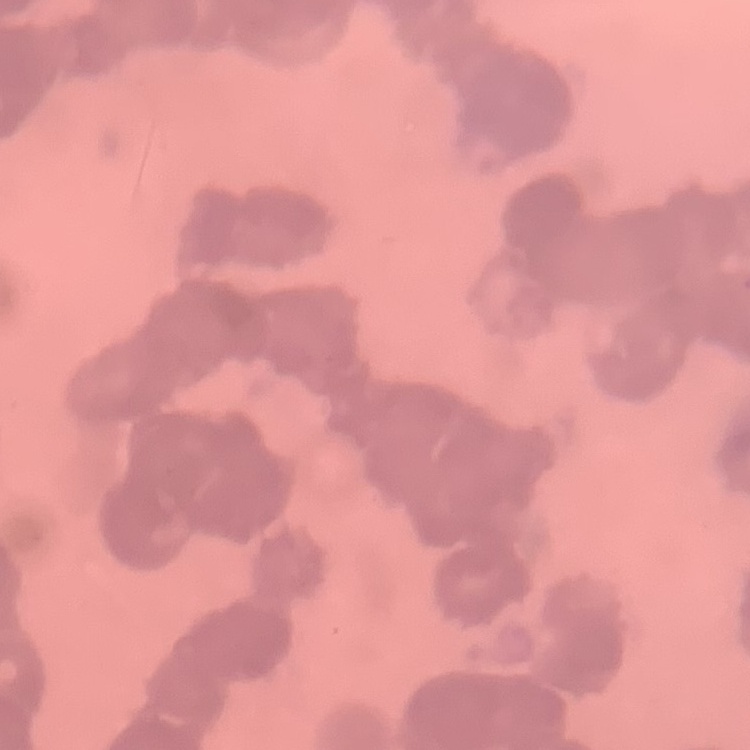

{
  "erythrocyte_morphology": "rouleaux formation",
  "stain": "Field's or Giemsa",
  "preparation": "thin blood smear",
  "image_type": "square crop of a larger photomicrograph"
}